Describe the morphology of the red blood cells.
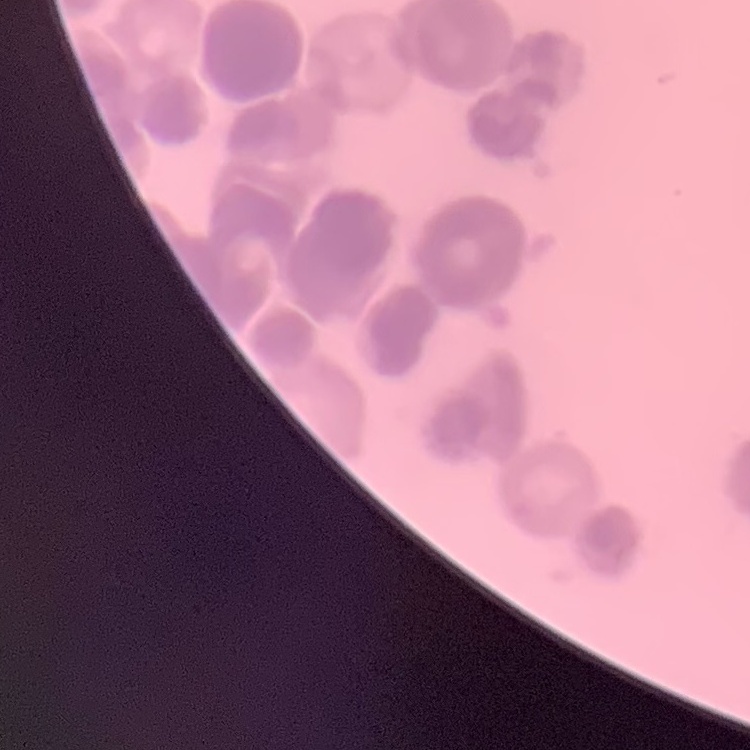
Rouleaux formation.

Summary:
  - Stain: Field's or Giemsa
  - Preparation: thin peripheral smear
  - Image type: square crop of a larger photomicrograph